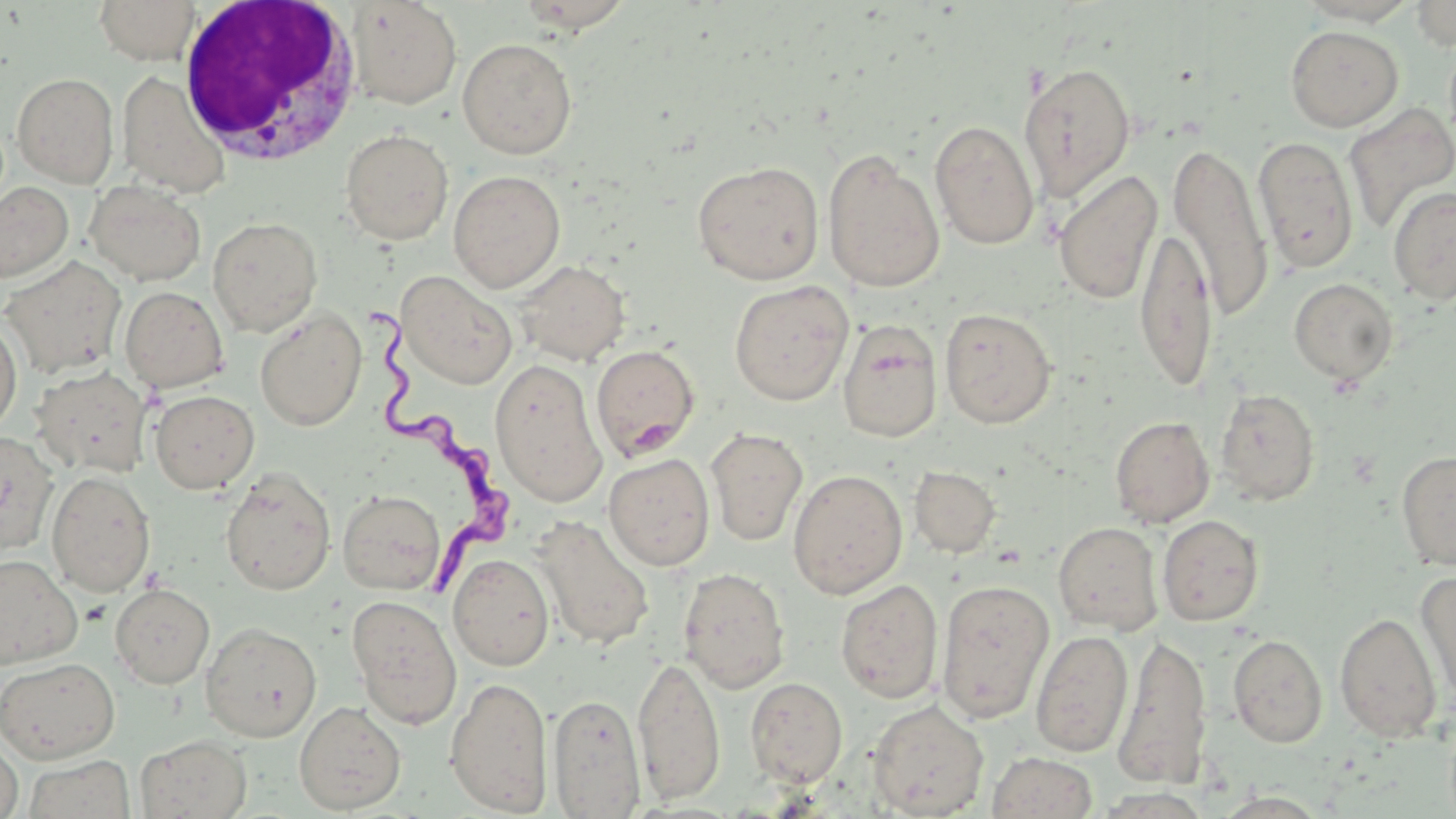

Approximate bounding boxes as (x1, y1, x2, y2) in pixels. White blood cell locations: (177, 0, 363, 166). Trypanosoma brucei locations: (359, 302, 507, 596). Uninfected red blood cell locations: (94, 0, 200, 64), (1410, 0, 1456, 50), (346, 1, 462, 109), (1285, 25, 1403, 132), (457, 38, 578, 159), (1018, 62, 1136, 200), (116, 70, 231, 197), (12, 72, 119, 187), (1343, 103, 1456, 233), (929, 119, 1039, 250), (340, 128, 453, 245), (1252, 136, 1359, 273), (1170, 141, 1273, 321), (822, 149, 945, 293), (692, 160, 825, 285), (448, 170, 565, 292), (1054, 170, 1163, 305), (85, 180, 206, 286), (0, 182, 74, 282), (1388, 185, 1456, 305), (207, 216, 323, 337), (1136, 224, 1217, 394), (0, 255, 127, 379), (514, 259, 631, 366), (396, 271, 518, 389), (1289, 277, 1399, 386), (729, 280, 853, 406), (119, 286, 228, 392), (254, 306, 367, 432), (939, 307, 1056, 428), (0, 317, 22, 436), (837, 319, 943, 443), (591, 344, 700, 461), (489, 358, 607, 506), (31, 366, 154, 479), (1215, 387, 1320, 505), (149, 389, 259, 493), (1110, 415, 1215, 528), (706, 427, 808, 546), (0, 429, 59, 556), (1396, 449, 1456, 571), (603, 453, 715, 571), (910, 465, 1001, 557), (220, 468, 336, 596), (788, 468, 907, 599), (47, 471, 155, 596), (338, 489, 445, 595), (1157, 514, 1264, 626), (532, 516, 654, 650), (1053, 521, 1163, 634), (448, 553, 555, 671), (0, 555, 82, 669), (678, 567, 790, 693), (1415, 571, 1456, 706), (835, 578, 944, 704), (936, 578, 1054, 723), (110, 583, 215, 689), (347, 594, 462, 729), (1334, 611, 1442, 743), (200, 621, 322, 742), (1031, 629, 1133, 757), (1113, 631, 1212, 789), (1228, 634, 1327, 748), (633, 655, 726, 805), (0, 657, 120, 763), (444, 676, 554, 815), (746, 677, 848, 788), (548, 692, 645, 817), (868, 699, 989, 817), (294, 700, 406, 814), (135, 734, 252, 819), (0, 738, 23, 819), (987, 751, 1097, 819), (23, 754, 135, 819). Slide-level diagnosis: Trypanosoma brucei. Single field of view. Image is 1456×819 pixels. May-Grünwald-Giemsa-stained preparation. Captured at 1000x magnification. Thin blood smear. Light microscopy.